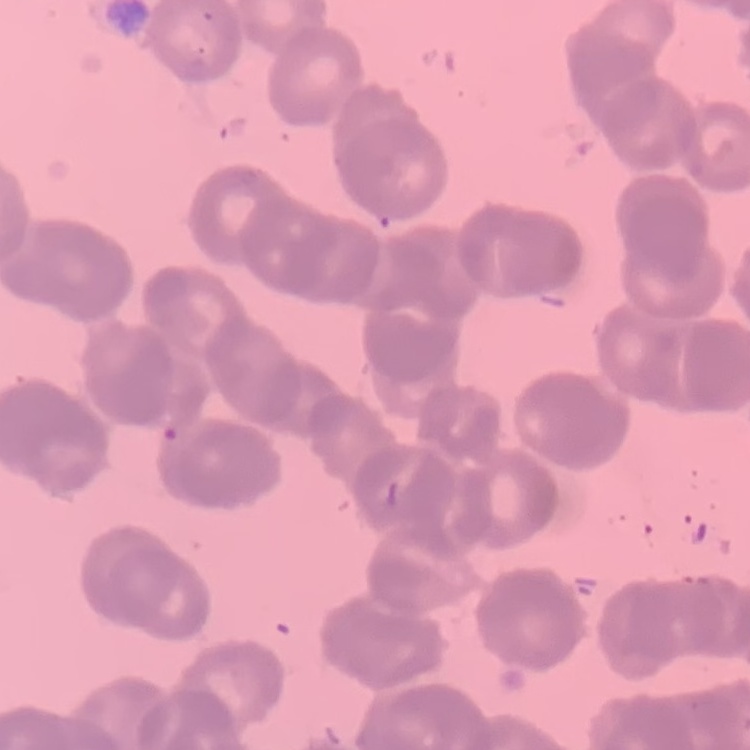 The erythrocytes show rouleaux formation. Field's or Giemsa stain. Square crop of a larger photomicrograph. Thin blood smear.